Name the parasite shown.
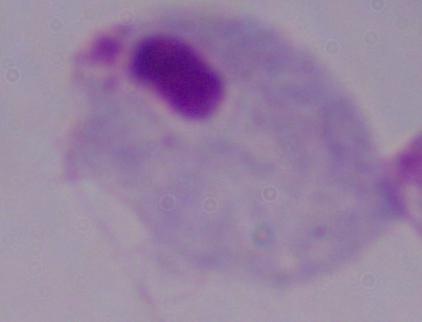

A trichomonad.

modality = photomicrograph
magnification = 1000x